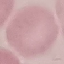
{
  "result": "no malaria parasites seen",
  "image_type": "automatically extracted cell patch, resized to 64 × 64 pixels",
  "preparation": "thin blood smear",
  "capture": "smartphone through the microscope eyepiece",
  "stain": "Giemsa"
}